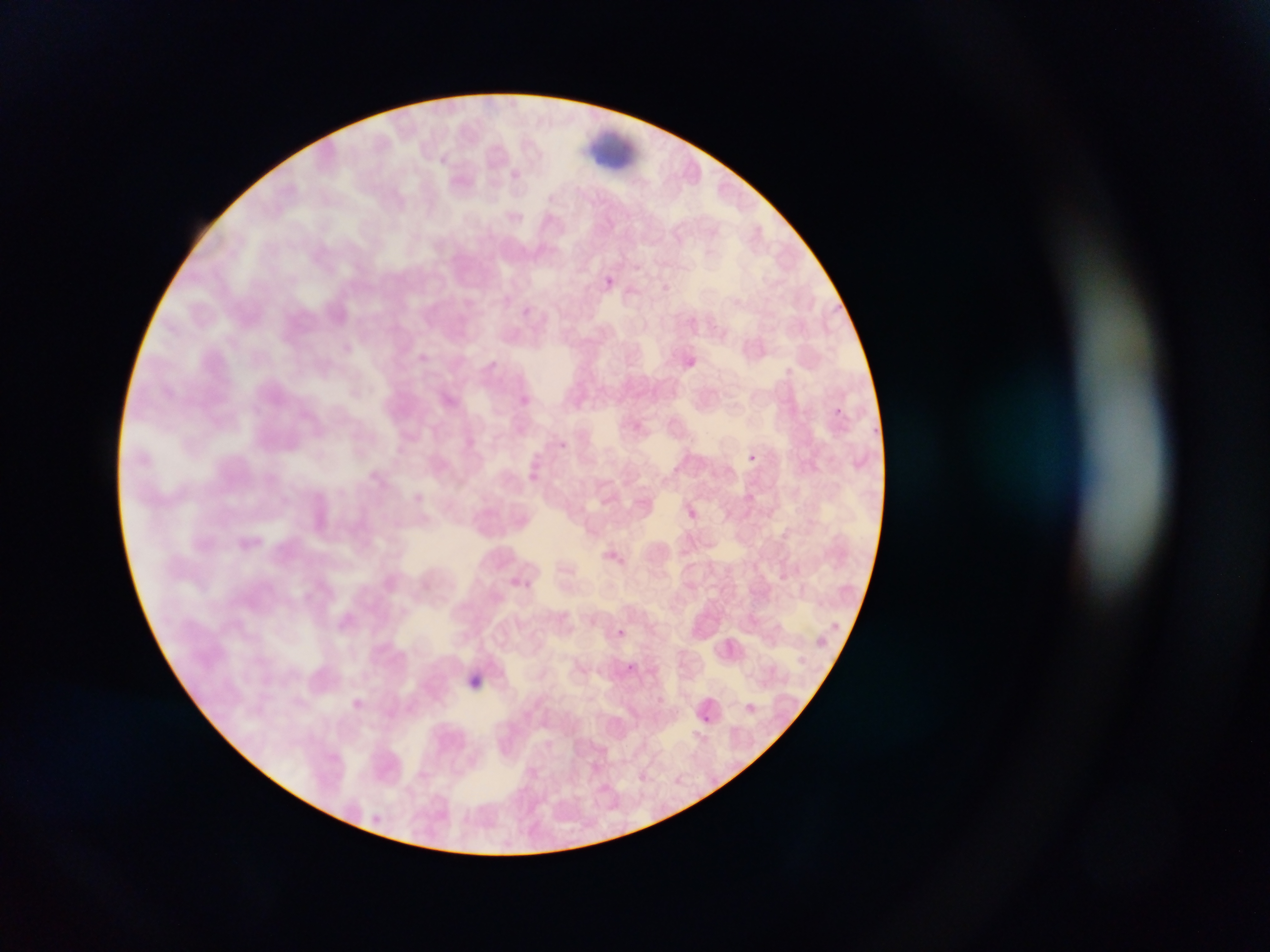

image_size: 1270×952 pixels
artifact_stain_precipitate_or_debris_locations: 'approximate bounding boxes as (left, top, right, bottom) in pixels: (576, 127, 634, 171)'
preparation: thin blood smear
malaria_parasite_locations: 'approximate bounding boxes as (left, top, right, bottom) in pixels: (600, 274, 617, 291), (827, 405, 845, 420), (557, 443, 571, 453), (749, 450, 762, 470), (683, 505, 701, 522), (525, 580, 539, 599), (611, 626, 628, 640), (627, 663, 636, 670), (467, 672, 484, 690), (704, 716, 712, 724)'
field_of_view: single
capture: mobile-phone photograph through a microscope
country: Ghana